Outline each blood parasite and name the species.
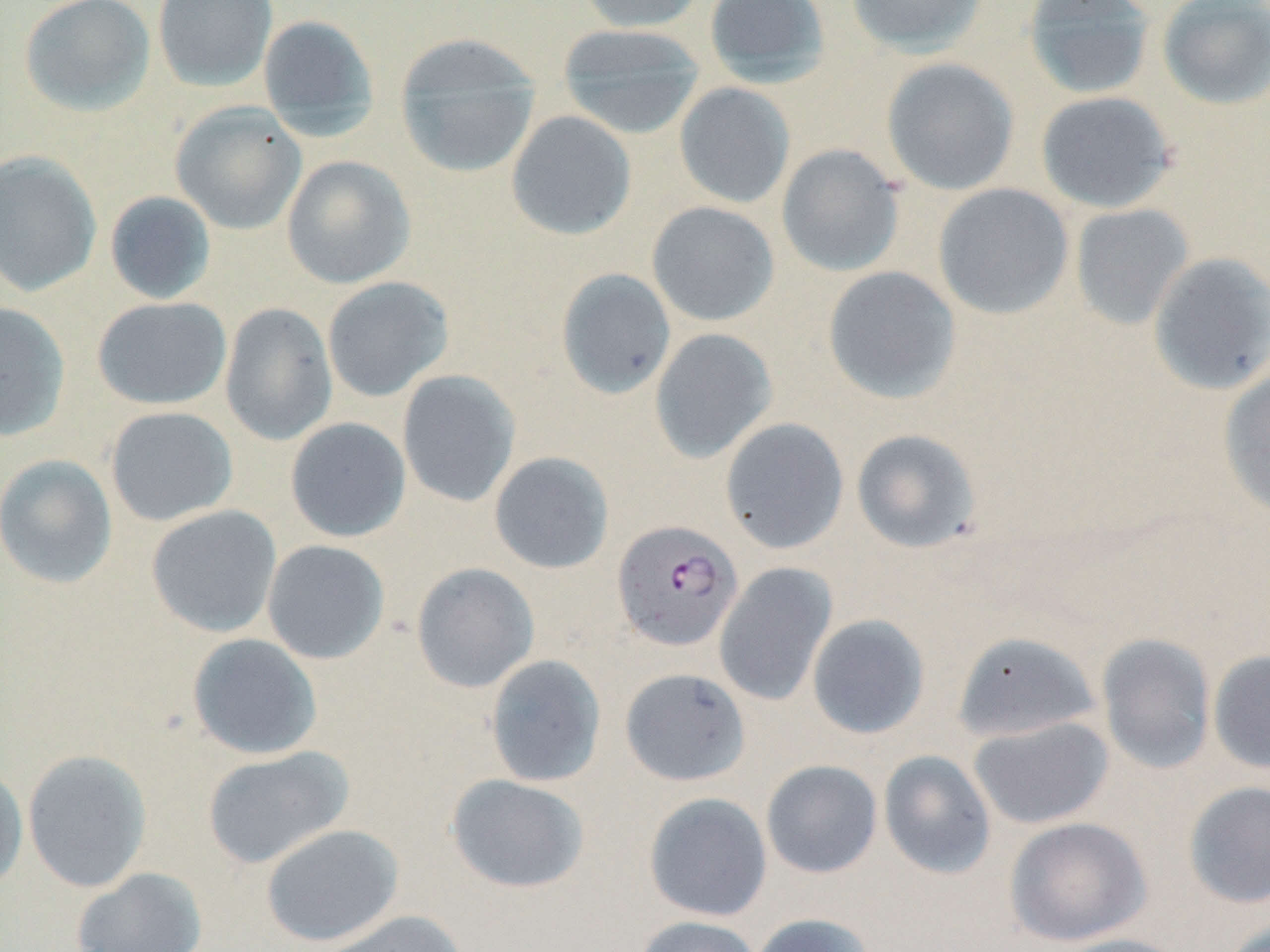

Approximate bounding boxes as [x1, y1, x2, y2] in pixels.
Plasmodium falciparum-infected red blood cells: [612, 519, 743, 652].
No Plasmodium ovale, Plasmodium malariae, Plasmodium vivax, Babesia divergens, or Trypanosoma brucei observed.

Summary:
  - Uninfected red blood cell locations: [19, 0, 156, 116], [153, 0, 278, 92], [575, 0, 706, 33], [703, 0, 831, 86], [846, 0, 988, 58], [1022, 0, 1156, 100], [1156, 1, 1270, 109], [257, 14, 380, 138], [556, 22, 705, 139], [394, 33, 541, 178], [881, 58, 1020, 196], [674, 82, 796, 209], [1035, 90, 1178, 213], [170, 101, 307, 235], [506, 110, 637, 241], [776, 144, 904, 278], [0, 151, 102, 297], [281, 155, 416, 288], [933, 183, 1074, 319], [104, 191, 217, 305], [646, 201, 780, 327], [1069, 203, 1194, 330], [1147, 252, 1270, 395], [822, 266, 962, 405], [555, 268, 676, 399], [321, 276, 454, 402], [92, 297, 232, 410], [0, 301, 71, 441], [219, 302, 338, 446], [649, 328, 778, 463], [1217, 368, 1270, 518], [397, 370, 521, 508], [105, 406, 238, 527], [285, 417, 411, 542], [719, 418, 850, 555], [851, 429, 982, 553], [489, 451, 614, 574], [0, 454, 118, 588], [146, 505, 282, 637], [262, 540, 390, 664], [410, 562, 540, 693], [714, 562, 837, 707], [807, 614, 930, 739], [952, 630, 1102, 742], [187, 633, 323, 760], [1096, 633, 1217, 774], [1208, 650, 1270, 775], [484, 654, 607, 787], [619, 667, 751, 786], [968, 716, 1114, 829], [201, 746, 354, 869], [22, 749, 152, 892], [878, 750, 997, 879], [761, 759, 882, 878], [0, 765, 29, 893], [445, 774, 590, 895], [1183, 780, 1270, 909], [643, 792, 773, 922], [1004, 816, 1151, 946], [261, 823, 404, 947], [71, 867, 208, 952], [315, 909, 468, 952], [748, 912, 876, 952], [632, 915, 763, 952], [1220, 918, 1270, 952], [1049, 933, 1191, 952]
  - Slide-level diagnosis: Plasmodium falciparum
  - Modality: optical microscopy
  - Stain: May-Grünwald-Giemsa
  - Preparation: thin blood smear
  - Field of view: single
  - Magnification: 1000x
  - Image size: 1270×952 pixels